Identify the parasite.
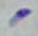
Toxoplasma gondii.

Captured at 1000x magnification. Micrograph.